Assess this cell for malaria.
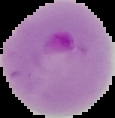
It is parasitized.

From a thin blood film. Segmented cell region on a black background. Image is 115×118 pixels.